Locate every Plasmodium parasite.
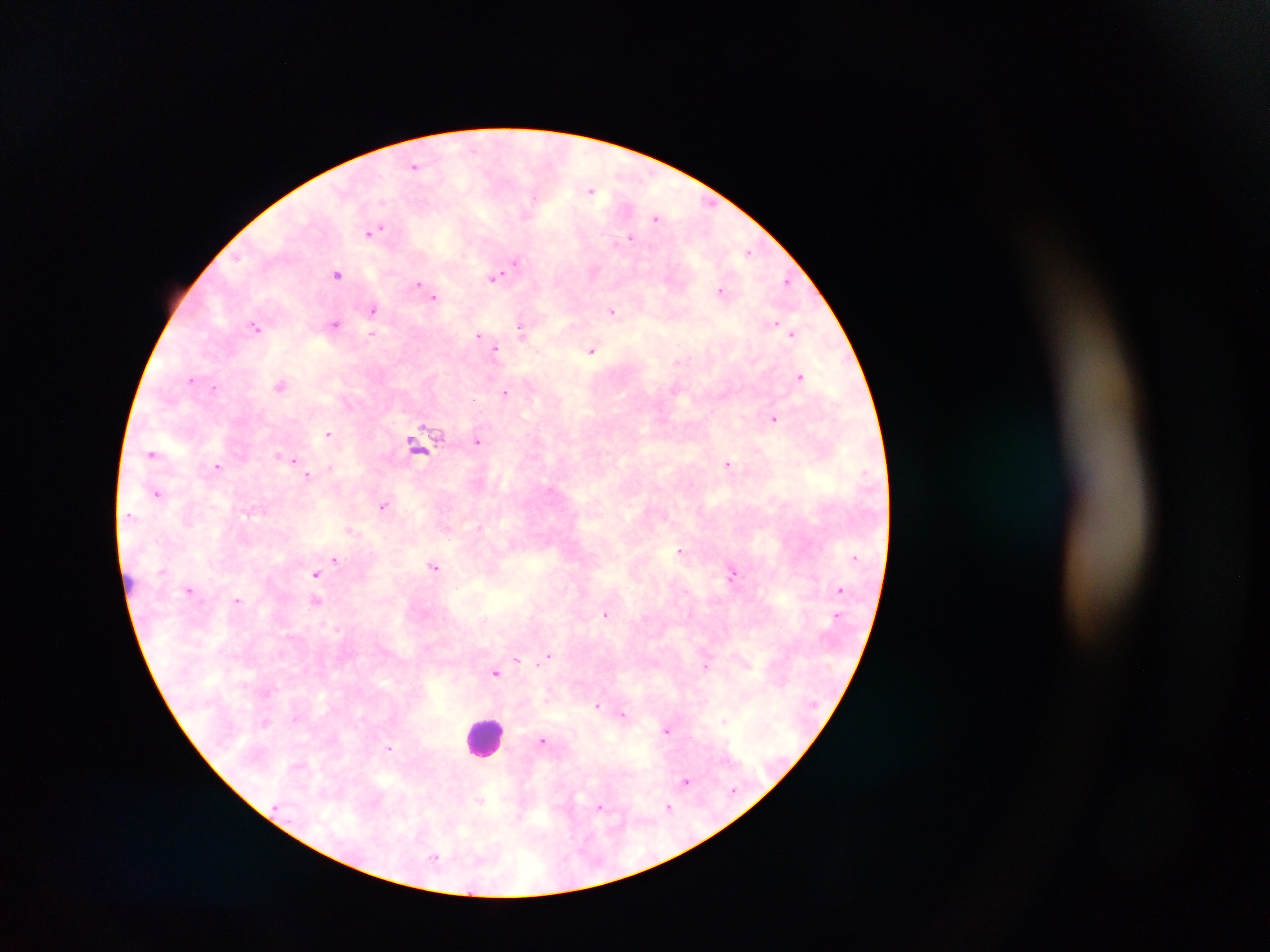
Approximate centers as x y in pixels.
Plasmodium parasites: 415 166; 591 190; 657 217; 376 230; 630 238; 748 252; 516 262; 338 274; 494 277; 786 281; 418 284; 721 291; 434 297; 373 308; 612 311; 776 323; 335 324; 256 327; 522 330; 373 334; 792 334; 479 335; 495 348; 538 351; 591 351; 680 362; 800 376; 190 379; 281 385; 215 388; 674 389; 505 391; 774 419; 328 433; 477 442; 420 447; 151 453; 286 457; 292 459; 297 464; 728 465; 217 466; 308 476; 156 493; 383 505; 129 515; 351 530; 680 550; 335 559; 435 567; 315 574; 732 574; 840 589; 190 590; 238 600; 315 601; 606 614; 549 655; 518 660; 706 665; 495 673; 597 705; 622 714; 724 721; 667 730; 543 741; 389 747; 686 782; 479 800; 600 806; 669 807; 435 857.

Leukocyte locations: 486 734. Sample from Ghana. Image is 1270×952 pixels. Photographed through a microscope with a mobile-phone camera. Single field of view. Thick blood film.